Name the blood parasite species.
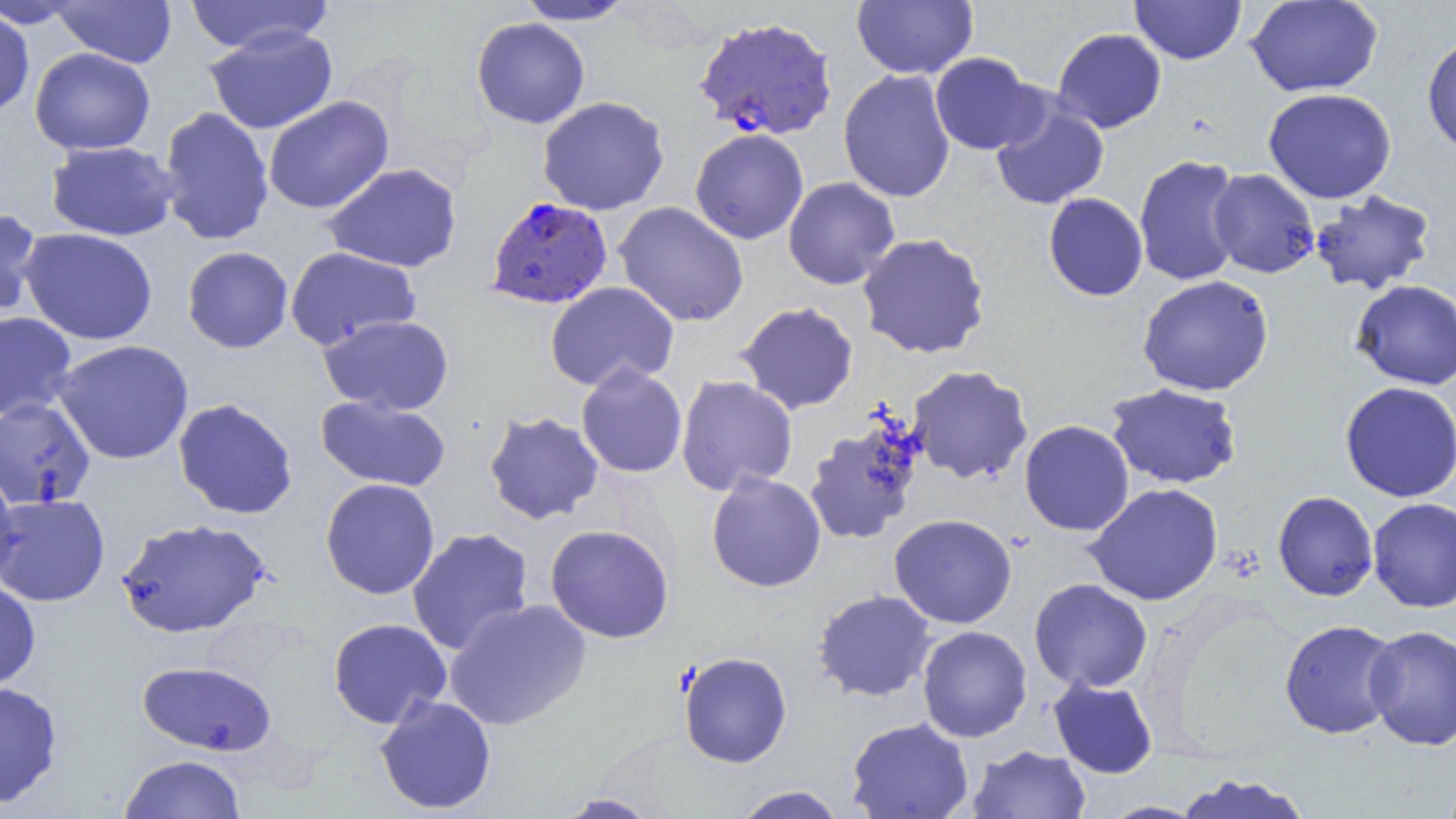

Plasmodium falciparum.

Approximate bounding boxes as named x1/y1/x2/y2 corners in pixels. Plasmodium falciparum-infected red blood cell locations: (x1=692, y1=16, x2=838, y2=141), (x1=485, y1=196, x2=613, y2=309). Uninfected red blood cell locations: (x1=51, y1=0, x2=177, y2=68), (x1=182, y1=0, x2=334, y2=55), (x1=513, y1=0, x2=639, y2=25), (x1=1129, y1=0, x2=1247, y2=64), (x1=1245, y1=0, x2=1383, y2=97), (x1=1, y1=1, x2=85, y2=29), (x1=851, y1=1, x2=978, y2=80), (x1=0, y1=7, x2=35, y2=118), (x1=471, y1=17, x2=590, y2=129), (x1=203, y1=26, x2=338, y2=134), (x1=1052, y1=28, x2=1167, y2=133), (x1=1421, y1=32, x2=1456, y2=156), (x1=29, y1=47, x2=155, y2=155), (x1=929, y1=52, x2=1042, y2=155), (x1=838, y1=69, x2=956, y2=203), (x1=1263, y1=88, x2=1397, y2=204), (x1=263, y1=95, x2=394, y2=215), (x1=989, y1=95, x2=1110, y2=210), (x1=537, y1=96, x2=670, y2=216), (x1=158, y1=106, x2=274, y2=246), (x1=689, y1=128, x2=809, y2=245), (x1=45, y1=140, x2=179, y2=241), (x1=1133, y1=154, x2=1245, y2=287), (x1=322, y1=163, x2=463, y2=273), (x1=1208, y1=168, x2=1320, y2=279), (x1=783, y1=177, x2=901, y2=290), (x1=1309, y1=189, x2=1436, y2=295), (x1=1043, y1=193, x2=1148, y2=301), (x1=613, y1=201, x2=750, y2=327), (x1=0, y1=207, x2=43, y2=322), (x1=18, y1=227, x2=158, y2=346), (x1=857, y1=233, x2=991, y2=360), (x1=182, y1=246, x2=293, y2=353), (x1=284, y1=246, x2=421, y2=351), (x1=1137, y1=274, x2=1274, y2=396), (x1=1351, y1=279, x2=1456, y2=390), (x1=545, y1=281, x2=680, y2=392), (x1=735, y1=301, x2=859, y2=415), (x1=0, y1=311, x2=77, y2=422), (x1=320, y1=315, x2=455, y2=416), (x1=53, y1=339, x2=195, y2=465), (x1=576, y1=363, x2=688, y2=479), (x1=907, y1=364, x2=1033, y2=485), (x1=675, y1=375, x2=798, y2=496), (x1=1339, y1=381, x2=1456, y2=502), (x1=1104, y1=382, x2=1243, y2=489), (x1=315, y1=395, x2=451, y2=493), (x1=0, y1=396, x2=96, y2=510), (x1=173, y1=398, x2=298, y2=520), (x1=484, y1=411, x2=605, y2=525), (x1=803, y1=416, x2=926, y2=546), (x1=1019, y1=420, x2=1134, y2=537), (x1=0, y1=463, x2=20, y2=592), (x1=706, y1=472, x2=826, y2=593), (x1=320, y1=478, x2=440, y2=600), (x1=1085, y1=482, x2=1224, y2=606), (x1=1272, y1=491, x2=1378, y2=601), (x1=0, y1=493, x2=110, y2=606), (x1=1367, y1=497, x2=1456, y2=612), (x1=889, y1=513, x2=1017, y2=629), (x1=114, y1=517, x2=273, y2=639), (x1=545, y1=523, x2=674, y2=644), (x1=406, y1=527, x2=535, y2=656), (x1=0, y1=578, x2=41, y2=692), (x1=1029, y1=578, x2=1153, y2=693), (x1=811, y1=589, x2=937, y2=703), (x1=443, y1=598, x2=593, y2=731), (x1=327, y1=617, x2=452, y2=730), (x1=1279, y1=619, x2=1402, y2=739), (x1=1364, y1=624, x2=1456, y2=750), (x1=917, y1=625, x2=1033, y2=742), (x1=678, y1=651, x2=793, y2=768), (x1=136, y1=660, x2=277, y2=756), (x1=1047, y1=676, x2=1158, y2=779), (x1=0, y1=680, x2=63, y2=808), (x1=374, y1=694, x2=498, y2=815), (x1=846, y1=716, x2=974, y2=819), (x1=966, y1=745, x2=1091, y2=819), (x1=118, y1=754, x2=246, y2=819), (x1=1175, y1=773, x2=1312, y2=819), (x1=730, y1=785, x2=847, y2=819), (x1=551, y1=793, x2=662, y2=818), (x1=1099, y1=801, x2=1207, y2=819). Image is 1456×819 pixels. 1000x magnification. Thin blood film. Single field of view. Optical microscopy.